Report the malaria status of this cell.
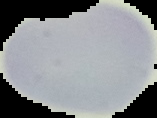
It is uninfected.

image_size: 157×118 pixels
preparation: thin blood film
image_type: cell region segmented out of the field of view; surrounding area masked to black